Classify this cell by malaria status.
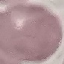
Uninfected.

{
  "image_type": "cell patch, automatically extracted from a larger field of view and resized to 64 × 64 pixels",
  "preparation": "thin blood smear",
  "stain": "Giemsa",
  "capture": "smartphone camera at the microscope eyepiece"
}